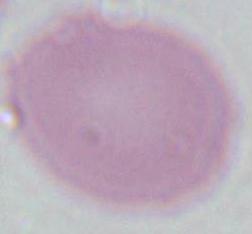

Summary:
  - Magnification: 1000x
  - Modality: photomicrograph
  - Identification: erythrocyte